Assess this cell for malaria.
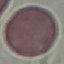
It is uninfected.

Summary:
  - Capture: smartphone camera at the microscope eyepiece
  - Stain: Giemsa
  - Image type: cell patch, automatically extracted from a larger field of view and resized to 64 × 64 pixels
  - Preparation: thin blood film